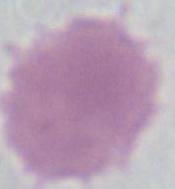

A red blood cell is seen. Micrograph. 1000x magnification.